State the blood parasite species.
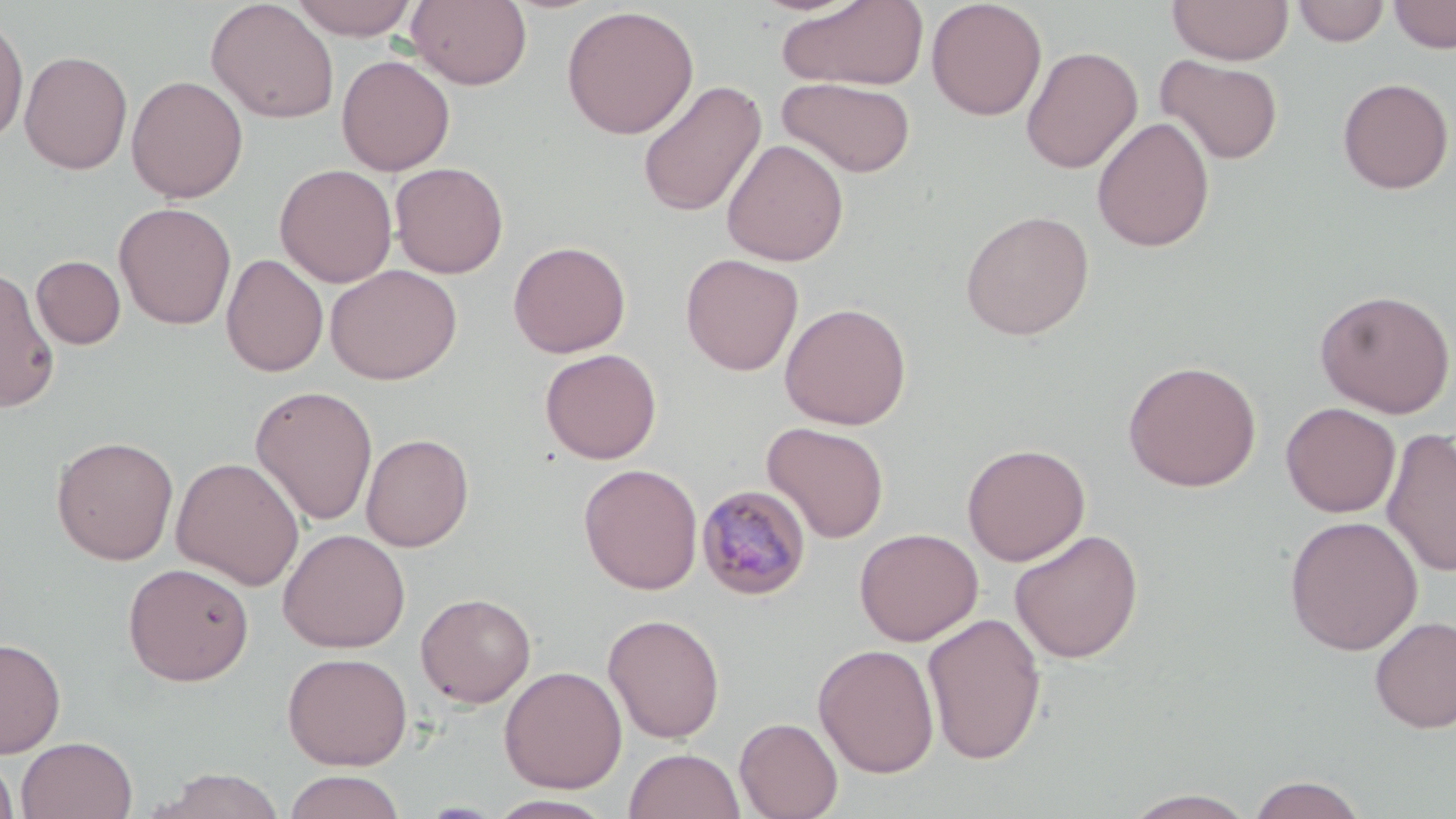

Plasmodium malariae.

Approximate bounding boxes as [x1, y1, x2, y2] in pixels. Plasmodium malariae-infected red blood cell locations: [695, 484, 813, 601]. Uninfected red blood cell locations: [288, 0, 419, 40], [406, 0, 532, 90], [775, 0, 929, 92], [926, 0, 1047, 121], [1166, 0, 1294, 66], [1388, 0, 1455, 53], [205, 1, 339, 124], [1292, 1, 1390, 46], [561, 5, 699, 139], [0, 11, 29, 146], [1020, 46, 1143, 174], [19, 50, 134, 175], [336, 54, 456, 176], [1156, 55, 1283, 165], [126, 75, 248, 203], [777, 77, 916, 177], [1336, 77, 1454, 194], [637, 80, 767, 218], [1091, 117, 1215, 253], [721, 138, 849, 267], [390, 162, 509, 278], [274, 164, 398, 288], [114, 202, 236, 329], [960, 210, 1094, 340], [508, 240, 631, 358], [221, 253, 329, 377], [680, 254, 803, 375], [32, 256, 126, 349], [325, 264, 462, 385], [0, 265, 60, 415], [1314, 289, 1455, 418], [779, 302, 911, 430], [540, 348, 662, 464], [1123, 360, 1261, 492], [249, 385, 378, 526], [1281, 402, 1401, 517], [762, 422, 889, 544], [1381, 427, 1456, 578], [360, 433, 474, 551], [51, 435, 179, 565], [961, 443, 1091, 566], [171, 457, 305, 590], [579, 463, 703, 595], [1283, 516, 1423, 656], [854, 527, 983, 646], [278, 528, 410, 652], [1008, 529, 1144, 663], [122, 561, 255, 687], [416, 592, 536, 708], [921, 612, 1047, 765], [602, 613, 726, 743], [1370, 615, 1456, 733], [0, 636, 66, 757], [812, 643, 940, 778], [282, 651, 413, 770], [499, 665, 627, 794], [734, 717, 843, 819], [16, 735, 138, 819], [624, 747, 745, 819], [0, 753, 19, 818], [150, 767, 286, 819], [282, 770, 407, 819], [1246, 774, 1368, 818], [1122, 788, 1258, 818], [485, 794, 619, 818]. Single field of view. Optical microscopy. May-Grünwald-Giemsa stain. Thin blood film. Captured at 1000x magnification. Image is 1456×819 pixels.